Name the parasite shown.
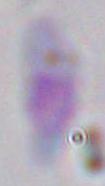

Toxoplasma gondii.

Captured at 1000x magnification. Micrograph.